Outline each Plasmodium ovale-infected red blood cell.
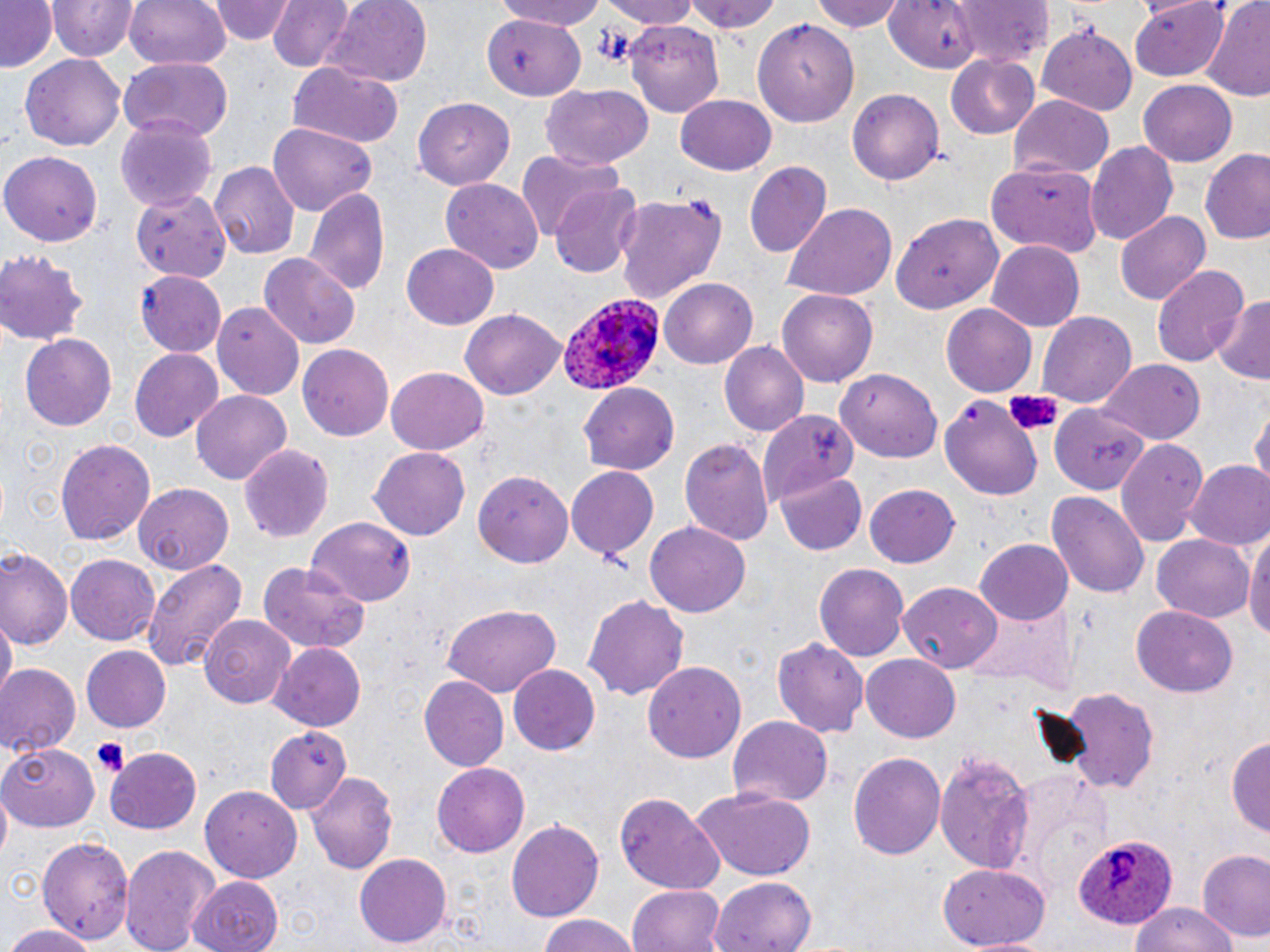

Approximate bounding boxes as [x1, y1, x2, y2] in pixels.
Plasmodium ovale-infected red blood cells: [554, 290, 666, 397], [1071, 835, 1180, 931].

slide_level_diagnosis: Plasmodium ovale
modality: optical microscopy
platelet_locations: 'approximate bounding boxes as [x1, y1, x2, y2] in pixels: [92, 738, 129, 777]'
uninfected_red_blood_cell_locations: 'approximate bounding boxes as [x1, y1, x2, y2] in pixels: [123, 0, 231, 73], [211, 0, 290, 44], [267, 0, 353, 71], [488, 0, 615, 29], [598, 0, 702, 26], [804, 0, 909, 33], [949, 0, 1054, 68], [1, 1, 59, 72], [45, 1, 137, 62], [685, 1, 783, 34], [887, 1, 984, 75], [1129, 1, 1232, 80], [1201, 1, 1270, 102], [321, 2, 433, 90], [485, 14, 586, 102], [753, 14, 857, 126], [626, 18, 725, 114], [1038, 24, 1139, 114], [20, 53, 126, 152], [947, 54, 1039, 139], [120, 57, 232, 141], [287, 62, 405, 148], [1138, 80, 1237, 165], [541, 84, 654, 167], [848, 88, 944, 186], [675, 95, 777, 175], [1009, 97, 1114, 180], [413, 100, 516, 187], [115, 117, 219, 210], [265, 122, 379, 212], [1087, 140, 1179, 242], [2, 150, 103, 246], [1200, 150, 1270, 246], [517, 151, 619, 240], [209, 160, 299, 260], [744, 161, 832, 257], [990, 162, 1100, 258], [440, 179, 544, 274], [551, 182, 641, 277], [305, 186, 391, 296], [128, 189, 234, 277], [616, 191, 725, 304], [783, 204, 898, 300], [893, 208, 1006, 314], [1116, 209, 1212, 304], [987, 241, 1084, 329], [401, 243, 499, 330], [0, 250, 90, 345], [259, 254, 358, 348], [1151, 264, 1249, 367], [136, 270, 227, 357], [660, 279, 756, 367], [776, 288, 879, 387], [1211, 296, 1270, 384], [212, 302, 307, 398], [940, 304, 1037, 395], [460, 308, 567, 399], [1039, 311, 1137, 405], [19, 333, 118, 430], [721, 341, 809, 437], [297, 344, 394, 440], [130, 350, 223, 441], [1097, 359, 1204, 442], [387, 366, 488, 451], [837, 372, 941, 462], [580, 380, 679, 471], [194, 390, 292, 485], [940, 394, 1043, 500], [1050, 402, 1150, 493], [1251, 408, 1270, 491], [755, 413, 854, 501], [679, 436, 775, 545], [54, 437, 155, 546], [1115, 440, 1208, 545], [238, 443, 335, 541], [370, 445, 470, 538], [1185, 460, 1270, 551], [566, 466, 658, 561], [473, 471, 574, 566], [775, 473, 868, 556], [866, 481, 961, 567], [133, 483, 232, 573], [1046, 491, 1150, 601], [307, 515, 415, 602], [644, 520, 752, 617], [1247, 522, 1270, 646], [1153, 534, 1254, 622], [975, 539, 1073, 626], [1, 548, 71, 650], [65, 554, 161, 645], [140, 558, 249, 672], [256, 558, 371, 653], [816, 563, 910, 664], [901, 581, 1005, 671], [582, 593, 691, 700], [967, 601, 1078, 688], [441, 604, 561, 696], [1130, 605, 1238, 696], [197, 614, 294, 707], [2, 615, 15, 702], [770, 635, 868, 738], [267, 643, 368, 731], [81, 647, 170, 733], [862, 652, 961, 740], [642, 661, 747, 762], [0, 664, 79, 758], [509, 666, 600, 755], [419, 675, 509, 769], [1058, 686, 1161, 791], [726, 716, 834, 809], [265, 727, 362, 819], [1228, 735, 1270, 845], [3, 742, 101, 832], [107, 746, 202, 834], [935, 748, 1036, 869], [848, 750, 946, 863], [431, 763, 531, 859], [308, 771, 398, 875], [1008, 772, 1111, 887], [199, 785, 302, 883], [691, 787, 817, 881], [615, 793, 725, 893], [505, 818, 603, 920], [38, 833, 135, 944], [121, 841, 216, 952], [1197, 849, 1270, 945], [355, 853, 452, 949], [936, 862, 1052, 949], [710, 874, 817, 950], [186, 876, 284, 952], [1162, 882, 1266, 952], [627, 884, 725, 952], [1126, 900, 1242, 952], [535, 915, 638, 952], [1, 924, 98, 952]'
field_of_view: one of a larger specimen
stain: May-Grünwald-Giemsa
preparation: thin blood film
magnification: 1000x
image_size: 1270×952 pixels